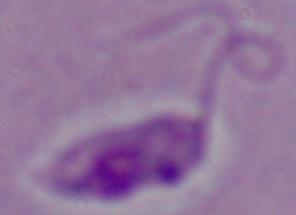

modality = micrograph
magnification = 1000x
identification = Leishmania